Comment on the morphology of the red blood cells.
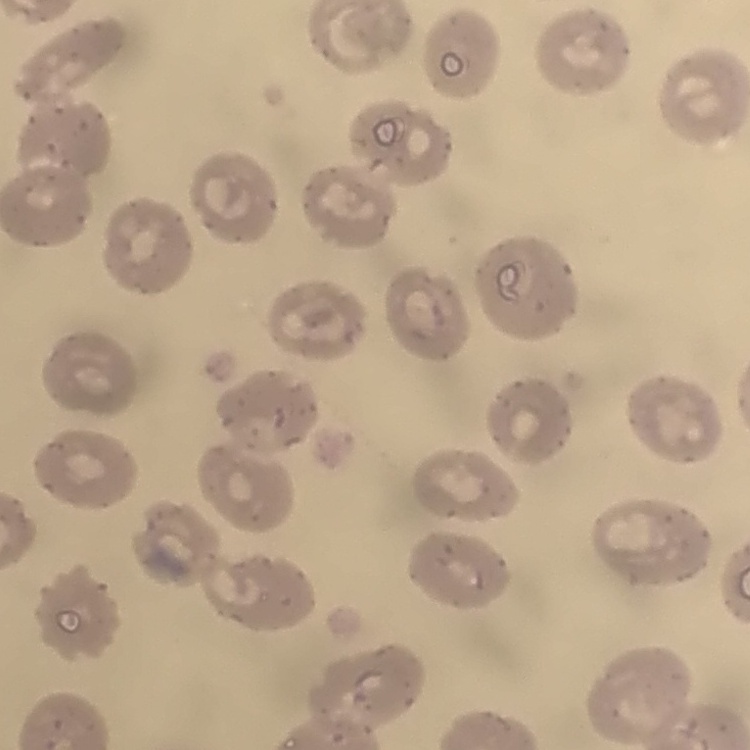

They show no rouleaux formation.

Square crop of a larger photomicrograph. Thin blood smear. Stained with either Field's or Giemsa.